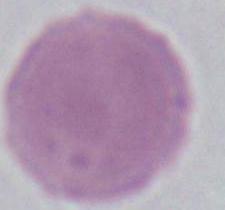
Summary:
  - Magnification: 1000x
  - Identification: erythrocyte
  - Modality: micrograph